Outline each blood parasite and name the species.
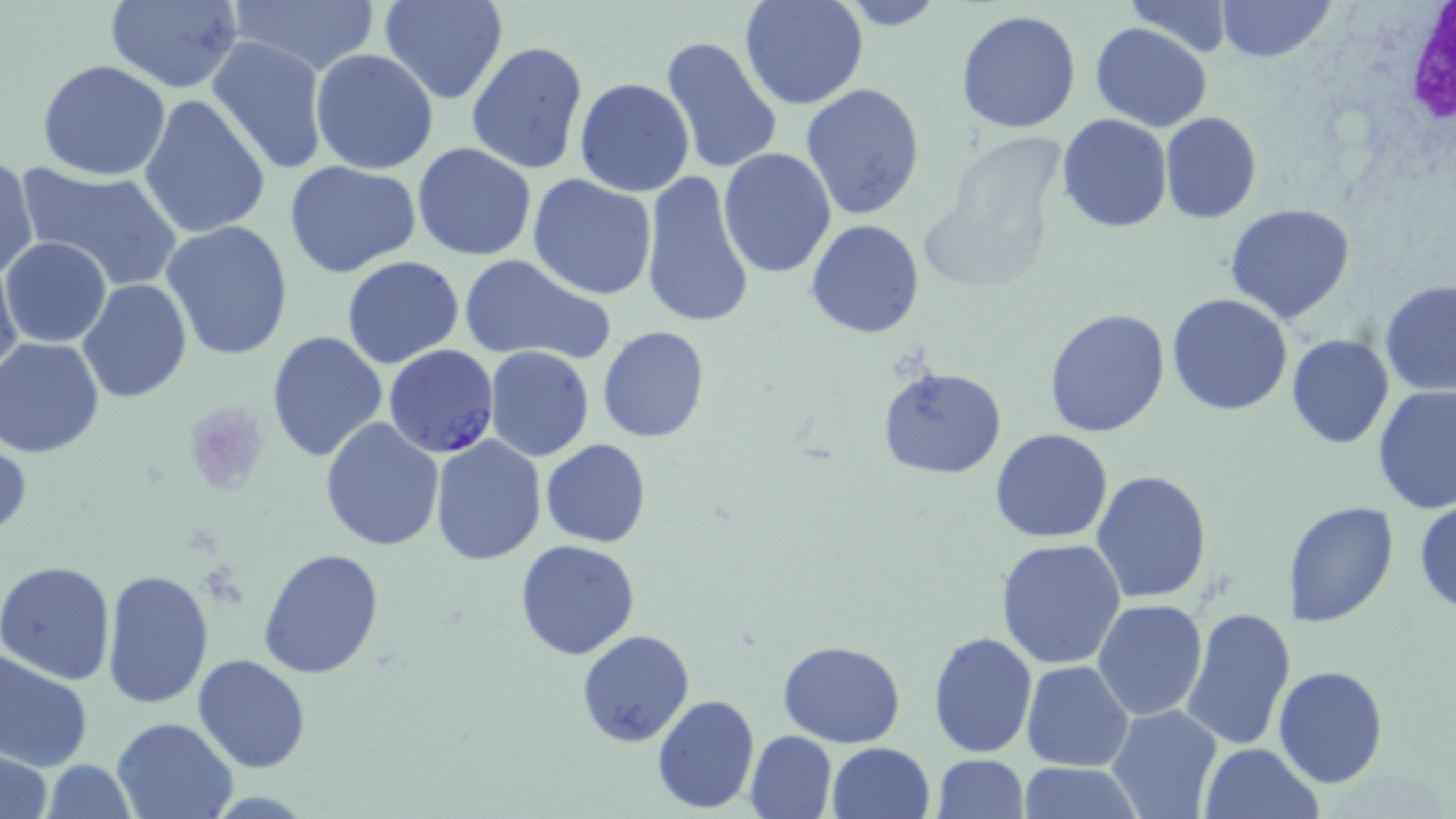
Approximate bounding boxes as (x1, y1, x2, y2) in pixels.
Plasmodium falciparum-infected red blood cells: (384, 344, 499, 459).
No Plasmodium ovale, Plasmodium malariae, Plasmodium vivax, Babesia divergens, or Trypanosoma brucei observed.

slide-level diagnosis = Plasmodium falciparum
modality = optical microscopy
white blood cell locations = approximate bounding boxes as (x1, y1, x2, y2) in pixels: (1395, 2, 1456, 186)
field of view = one of a larger specimen
image size = 1456×819 pixels
uninfected red blood cell locations = approximate bounding boxes as (x1, y1, x2, y2) in pixels: (104, 0, 245, 93), (228, 0, 381, 77), (379, 0, 509, 105), (741, 0, 869, 110), (832, 0, 947, 31), (1217, 0, 1333, 62), (1126, 1, 1233, 56), (956, 10, 1082, 134), (1090, 21, 1214, 131), (207, 36, 329, 175), (660, 36, 783, 177), (466, 41, 590, 177), (310, 49, 438, 175), (37, 59, 171, 181), (575, 77, 695, 198), (801, 82, 926, 220), (139, 94, 270, 240), (1159, 113, 1261, 225), (1056, 114, 1173, 234), (412, 143, 538, 261), (717, 149, 836, 279), (0, 156, 37, 285), (284, 159, 422, 279), (18, 165, 182, 292), (639, 170, 755, 331), (527, 174, 657, 299), (1224, 203, 1355, 324), (807, 219, 925, 338), (161, 220, 295, 360), (2, 237, 113, 348), (457, 254, 616, 366), (1, 257, 23, 383), (341, 257, 466, 370), (77, 278, 192, 405), (1378, 281, 1456, 397), (1167, 294, 1293, 415), (1043, 308, 1170, 437), (597, 327, 710, 444), (266, 330, 389, 466), (1286, 334, 1395, 450), (1, 338, 108, 458), (484, 346, 594, 461), (877, 363, 1007, 479), (1373, 385, 1456, 517), (321, 417, 445, 551), (990, 429, 1113, 544), (0, 436, 30, 545), (429, 436, 547, 565), (541, 438, 651, 548), (1091, 469, 1211, 604), (1415, 496, 1456, 619), (1284, 501, 1399, 629), (995, 538, 1127, 670), (513, 539, 640, 660), (259, 549, 385, 680), (0, 561, 118, 685), (101, 569, 214, 708), (1093, 600, 1209, 720), (1179, 605, 1297, 752), (928, 629, 1038, 759), (576, 630, 695, 747), (777, 640, 907, 747), (0, 648, 93, 771), (192, 655, 310, 773), (1022, 661, 1133, 770), (1274, 665, 1390, 788), (652, 695, 759, 812), (1107, 705, 1223, 818), (111, 716, 238, 818), (744, 730, 837, 819), (827, 741, 936, 819), (1198, 742, 1324, 819), (1, 749, 52, 819), (933, 755, 1028, 818), (42, 758, 137, 819), (1015, 762, 1143, 817)
preparation = thin blood smear
stain = May-Grünwald-Giemsa
magnification = 1000x
platelet locations = approximate bounding boxes as (x1, y1, x2, y2) in pixels: (182, 402, 267, 495)